Report the malaria status of this cell.
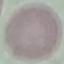

It is uninfected.

Thin blood film. Giemsa stain. Photographed with a smartphone camera at the microscope eyepiece. Automatically extracted cell patch, resized to 64 × 64 pixels.